Comment on the morphology of the erythrocytes.
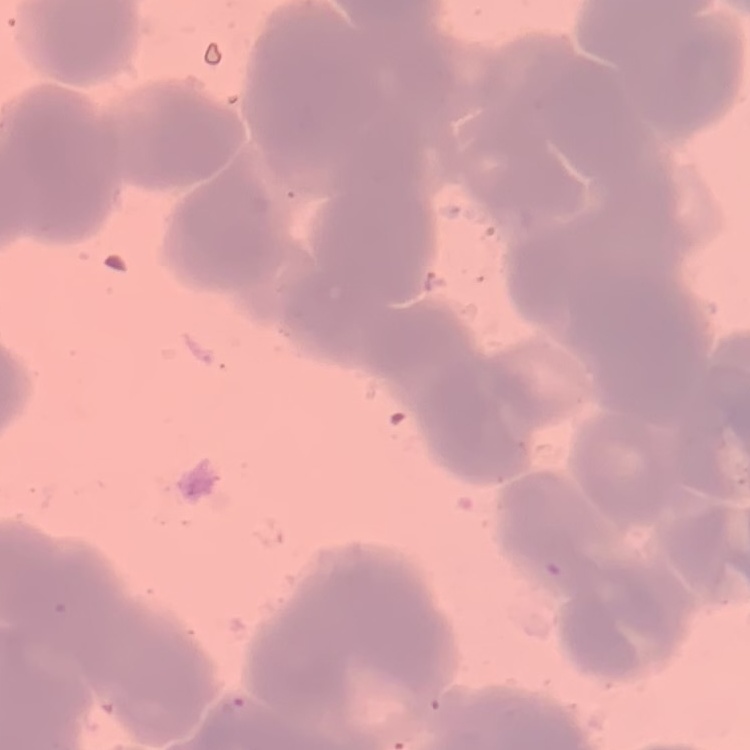
They show rouleaux formation.

Thin peripheral smear. Field's or Giemsa stain. Square crop of a larger photomicrograph.